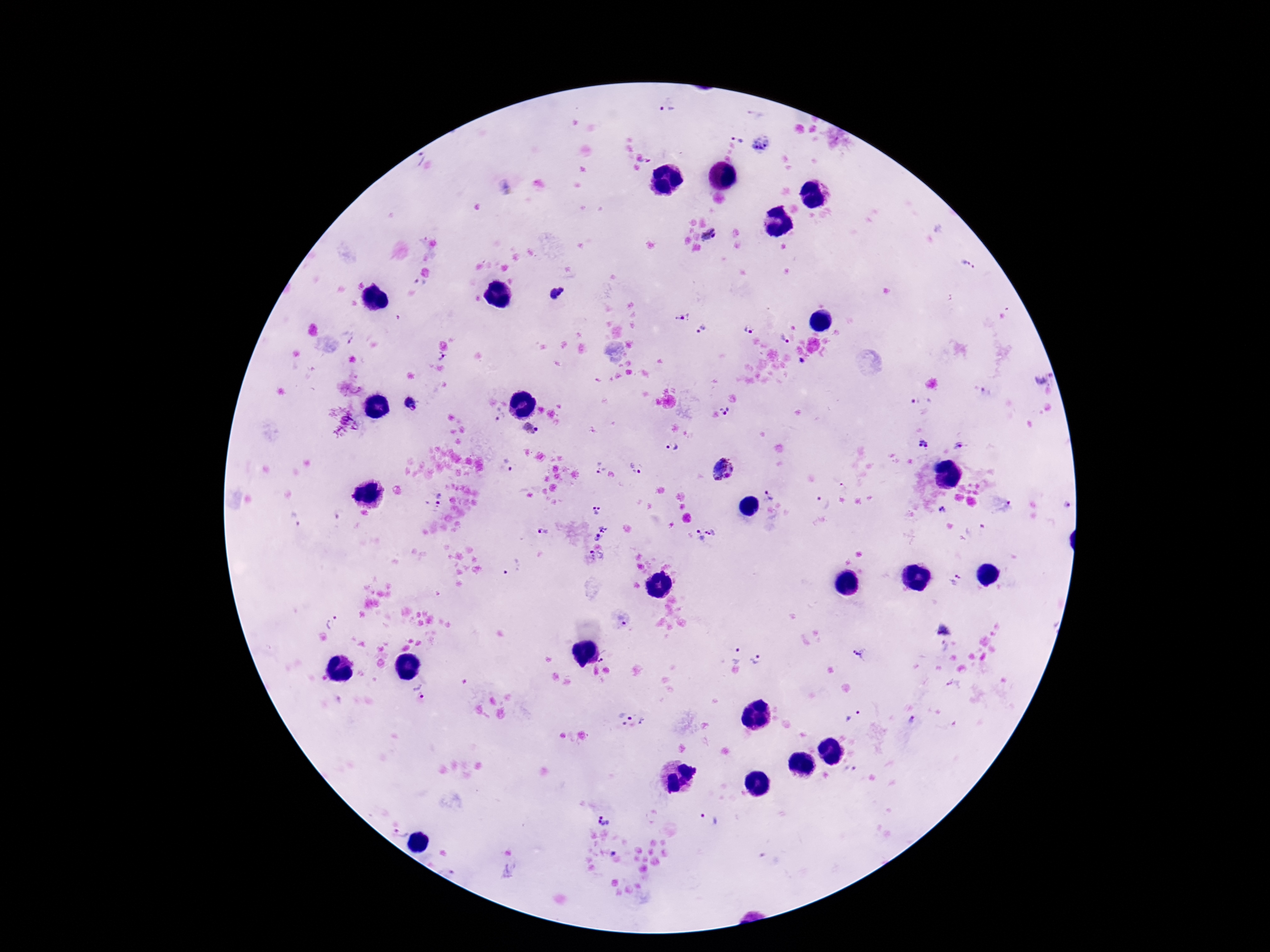

Approximate object centers, in pixels from the top-left corner.
Summary:
  - Plasmodium parasite locations: (x=667, y=109), (x=738, y=135), (x=760, y=144), (x=710, y=238), (x=969, y=264), (x=420, y=283), (x=557, y=293), (x=684, y=318), (x=703, y=329), (x=748, y=330), (x=347, y=336), (x=785, y=338), (x=441, y=357), (x=802, y=360), (x=1045, y=375), (x=921, y=401), (x=412, y=404), (x=725, y=411), (x=500, y=415), (x=529, y=429), (x=924, y=444), (x=672, y=446), (x=957, y=447), (x=509, y=466), (x=597, y=466), (x=637, y=467), (x=725, y=471), (x=843, y=487), (x=771, y=493), (x=437, y=500), (x=823, y=503), (x=1067, y=506), (x=596, y=509), (x=942, y=511), (x=606, y=529), (x=544, y=531), (x=710, y=531), (x=698, y=536), (x=597, y=539), (x=596, y=557), (x=512, y=567), (x=957, y=580), (x=622, y=619), (x=333, y=620), (x=736, y=655), (x=861, y=655), (x=602, y=660), (x=758, y=660), (x=419, y=689), (x=853, y=717), (x=631, y=718), (x=912, y=719), (x=851, y=768), (x=708, y=819), (x=604, y=821), (x=402, y=831)
  - Magnification: 100x
  - Field of view: one from this slide
  - Preparation: thick blood smear
  - Patient malaria status: positive
  - Stain: Giemsa
  - Image size: 1270×952 pixels
  - Capture: smartphone camera through the microscope eyepiece